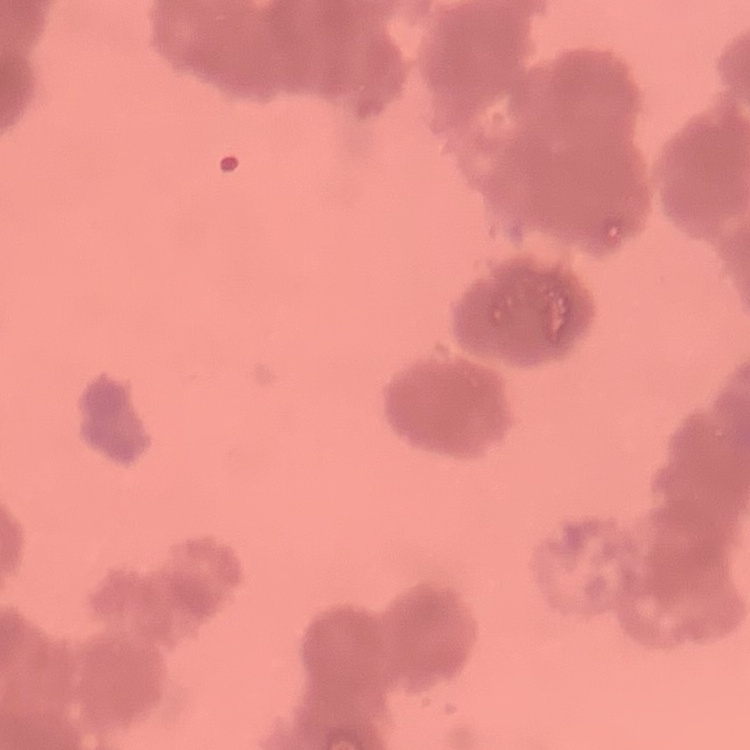
The red blood cells show rouleaux formation. Stained with either Field's or Giemsa. Thin blood film. One tile cut from a larger photomicrograph.